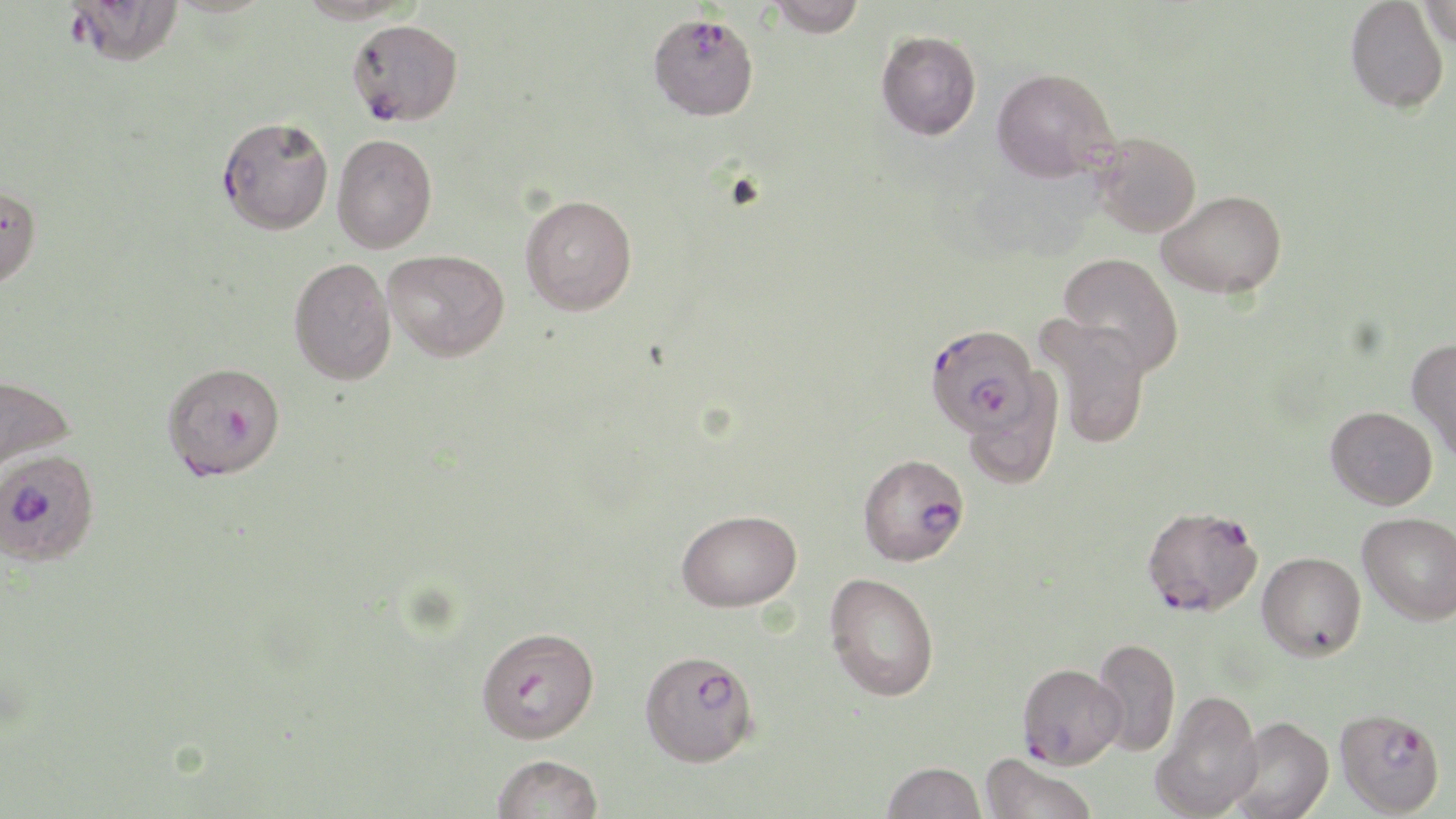 Approximate bounding boxes as [x1, y1, x2, y2] in pixels. Uninfected red blood cell locations: [66, 0, 184, 67], [295, 0, 419, 25], [768, 0, 866, 37], [1345, 0, 1449, 114], [1419, 0, 1456, 50], [876, 30, 981, 141], [991, 67, 1119, 183], [1092, 132, 1201, 237], [332, 133, 436, 253], [0, 183, 42, 291], [1157, 189, 1287, 299], [520, 194, 638, 315], [383, 249, 510, 362], [1057, 252, 1185, 377], [289, 257, 397, 385], [1036, 315, 1152, 449], [1407, 338, 1456, 464], [961, 370, 1065, 490], [0, 374, 75, 481], [1325, 406, 1437, 509], [676, 509, 802, 612], [1358, 512, 1456, 625], [1256, 551, 1366, 661], [824, 571, 940, 702], [1091, 637, 1180, 757], [1150, 690, 1263, 819], [1227, 716, 1334, 819], [980, 753, 1098, 819], [492, 754, 604, 818], [881, 760, 987, 819]. Plasmodium falciparum-infected red blood cell locations: [648, 12, 759, 120], [347, 19, 463, 126], [217, 115, 335, 234], [924, 323, 1042, 438], [162, 361, 286, 480], [858, 452, 970, 566], [1, 456, 99, 570], [1141, 504, 1263, 618], [476, 626, 599, 743], [639, 649, 759, 766], [1017, 662, 1126, 769], [1334, 708, 1445, 816]. Slide-level diagnosis: Plasmodium falciparum. Optical microscopy. Single field of view. 1000x magnification. Image is 1456×819 pixels. May-Grünwald-Giemsa stain. Thin blood film.